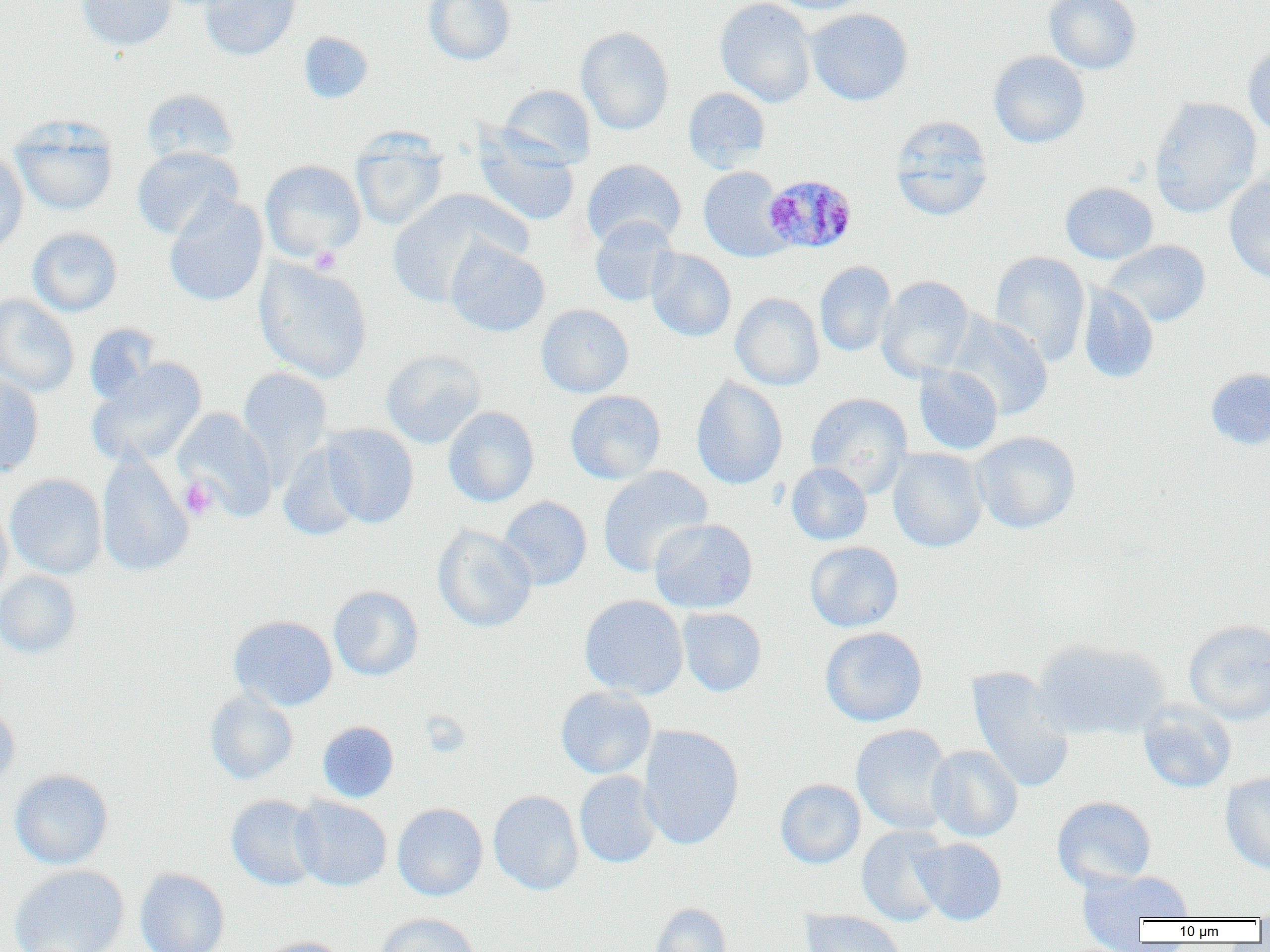

Summary:
  - Coordinate format: approximate bounding boxes as named x1/y1/x2/y2 corners in pixels
  - Uninfected red blood cell locations: (x1=75, y1=0, x2=178, y2=51), (x1=199, y1=0, x2=302, y2=60), (x1=423, y1=0, x2=515, y2=65), (x1=715, y1=0, x2=817, y2=107), (x1=768, y1=0, x2=874, y2=14), (x1=1044, y1=0, x2=1141, y2=74), (x1=805, y1=8, x2=913, y2=105), (x1=576, y1=26, x2=675, y2=135), (x1=298, y1=31, x2=374, y2=103), (x1=1243, y1=40, x2=1270, y2=139), (x1=988, y1=50, x2=1089, y2=148), (x1=499, y1=85, x2=596, y2=168), (x1=683, y1=87, x2=771, y2=172), (x1=140, y1=88, x2=240, y2=167), (x1=1148, y1=97, x2=1261, y2=217), (x1=10, y1=117, x2=119, y2=216), (x1=889, y1=117, x2=994, y2=221), (x1=473, y1=129, x2=580, y2=227), (x1=350, y1=131, x2=448, y2=231), (x1=131, y1=146, x2=243, y2=240), (x1=0, y1=150, x2=28, y2=256), (x1=581, y1=158, x2=686, y2=249), (x1=260, y1=160, x2=366, y2=261), (x1=698, y1=166, x2=792, y2=262), (x1=1224, y1=173, x2=1270, y2=283), (x1=1060, y1=182, x2=1158, y2=264), (x1=386, y1=189, x2=527, y2=307), (x1=164, y1=195, x2=268, y2=307), (x1=589, y1=217, x2=679, y2=307), (x1=27, y1=227, x2=122, y2=316), (x1=446, y1=239, x2=550, y2=337), (x1=1103, y1=239, x2=1211, y2=327), (x1=645, y1=248, x2=736, y2=342), (x1=990, y1=250, x2=1091, y2=365), (x1=254, y1=257, x2=373, y2=384), (x1=814, y1=261, x2=897, y2=356), (x1=876, y1=275, x2=975, y2=382), (x1=1078, y1=283, x2=1159, y2=383), (x1=0, y1=293, x2=80, y2=397), (x1=730, y1=293, x2=824, y2=390), (x1=536, y1=304, x2=633, y2=398), (x1=946, y1=311, x2=1053, y2=420), (x1=84, y1=323, x2=162, y2=405), (x1=381, y1=349, x2=486, y2=448), (x1=87, y1=358, x2=207, y2=469), (x1=913, y1=364, x2=1003, y2=455), (x1=238, y1=367, x2=333, y2=481), (x1=1205, y1=367, x2=1270, y2=449), (x1=0, y1=375, x2=44, y2=479), (x1=690, y1=376, x2=788, y2=489), (x1=565, y1=390, x2=666, y2=484), (x1=805, y1=392, x2=913, y2=495), (x1=443, y1=406, x2=539, y2=507), (x1=174, y1=408, x2=278, y2=519), (x1=322, y1=424, x2=419, y2=527), (x1=971, y1=431, x2=1081, y2=534), (x1=277, y1=441, x2=366, y2=541), (x1=887, y1=447, x2=988, y2=552), (x1=96, y1=452, x2=194, y2=577), (x1=786, y1=462, x2=872, y2=545), (x1=597, y1=466, x2=713, y2=577), (x1=5, y1=474, x2=107, y2=579), (x1=498, y1=496, x2=592, y2=590), (x1=0, y1=501, x2=13, y2=602), (x1=649, y1=518, x2=758, y2=613), (x1=432, y1=524, x2=537, y2=633), (x1=804, y1=541, x2=904, y2=632), (x1=0, y1=569, x2=81, y2=658), (x1=328, y1=585, x2=423, y2=681), (x1=579, y1=595, x2=688, y2=700), (x1=677, y1=607, x2=767, y2=696), (x1=228, y1=615, x2=338, y2=710), (x1=1184, y1=619, x2=1270, y2=724), (x1=820, y1=627, x2=928, y2=727), (x1=1032, y1=638, x2=1168, y2=740), (x1=967, y1=667, x2=1074, y2=794), (x1=555, y1=686, x2=657, y2=779), (x1=205, y1=689, x2=298, y2=784), (x1=0, y1=701, x2=20, y2=791), (x1=1138, y1=701, x2=1236, y2=793), (x1=318, y1=721, x2=399, y2=802), (x1=851, y1=724, x2=955, y2=835), (x1=638, y1=725, x2=744, y2=850), (x1=926, y1=745, x2=1023, y2=841), (x1=10, y1=769, x2=113, y2=869), (x1=574, y1=771, x2=661, y2=868), (x1=1220, y1=772, x2=1270, y2=874), (x1=775, y1=778, x2=866, y2=868), (x1=488, y1=790, x2=584, y2=895), (x1=226, y1=794, x2=322, y2=890), (x1=291, y1=796, x2=391, y2=891), (x1=1052, y1=796, x2=1156, y2=889), (x1=392, y1=802, x2=488, y2=901), (x1=856, y1=826, x2=952, y2=926), (x1=913, y1=837, x2=1007, y2=925), (x1=10, y1=864, x2=130, y2=952), (x1=134, y1=868, x2=230, y2=952), (x1=1077, y1=870, x2=1194, y2=930), (x1=651, y1=902, x2=732, y2=952), (x1=800, y1=909, x2=906, y2=952), (x1=375, y1=913, x2=480, y2=952), (x1=254, y1=937, x2=348, y2=952)
  - Plasmodium malariae-infected red blood cell locations: (x1=762, y1=174, x2=857, y2=254)
  - Platelet locations: (x1=309, y1=247, x2=341, y2=273), (x1=180, y1=477, x2=217, y2=520)
  - Slide-level diagnosis: Plasmodium malariae
  - Image size: 1270×952 pixels
  - Modality: optical microscopy
  - Magnification: 1000x
  - Preparation: thin blood film
  - Field of view: single